Give the position of every leukocyte visible.
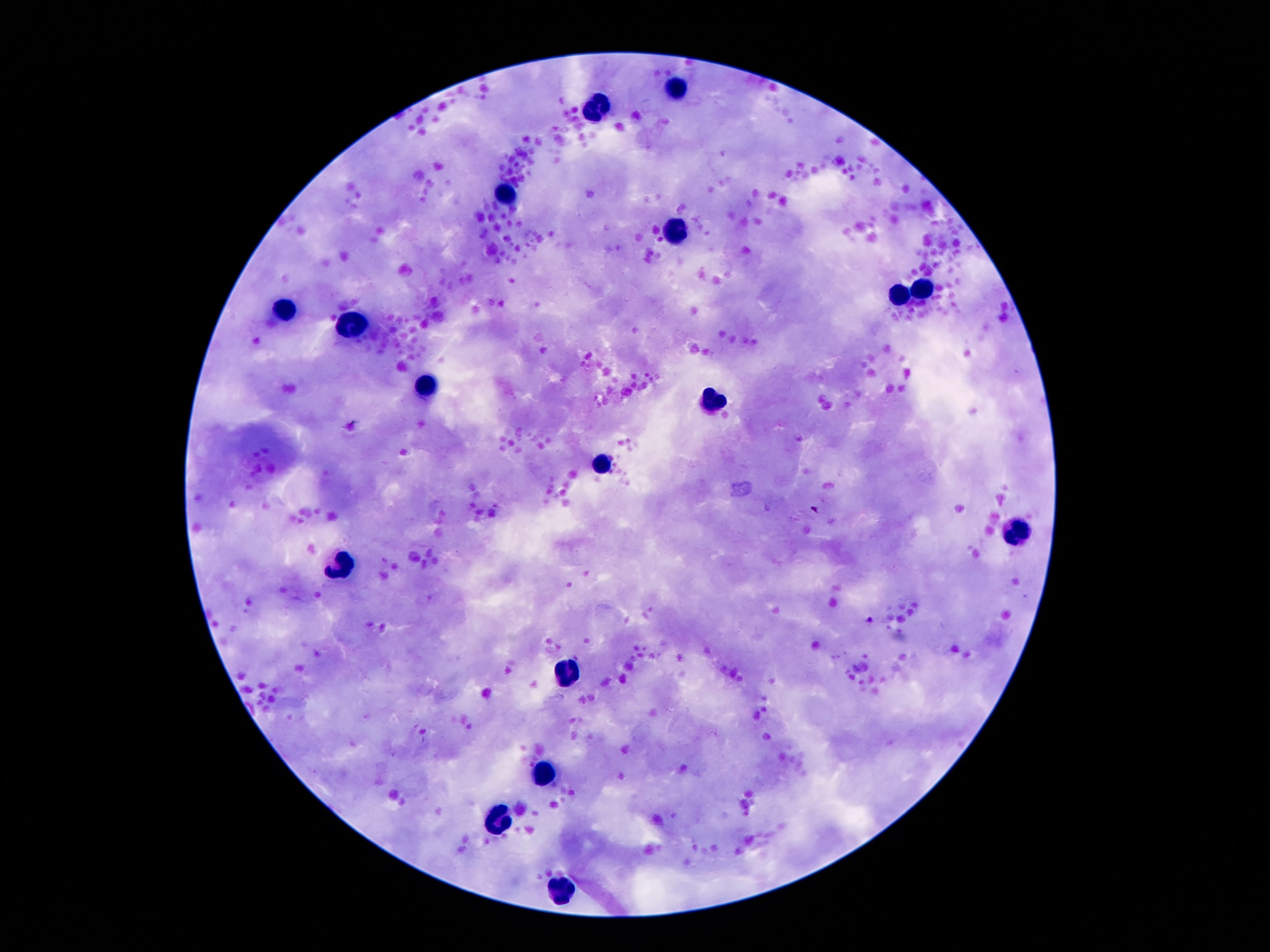

Approximate object centers, in pixels from the top-left corner.
Leukocytes: (x=680, y=90), (x=600, y=108), (x=504, y=195), (x=676, y=231), (x=921, y=284), (x=903, y=297), (x=285, y=311), (x=351, y=325), (x=426, y=385), (x=716, y=399), (x=602, y=465), (x=1018, y=529), (x=340, y=561), (x=567, y=675), (x=544, y=772), (x=500, y=818), (x=558, y=891).

{
  "image_size": "1270×952 pixels",
  "capture": "smartphone camera through the microscope eyepiece",
  "stain": "Giemsa",
  "field_of_view": "single",
  "magnification": "100x",
  "preparation": "thick peripheral-blood smear",
  "patient_malaria_status": "negative"
}